Classify this cell by malaria status.
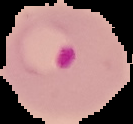
It is parasitized.

{
  "image_size": "133×124 pixels",
  "preparation": "thin blood smear",
  "image_type": "segmented cell region with the area outside set to black"
}